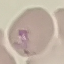

{
  "result": "no malaria parasites detected",
  "stain": "Giemsa",
  "image_type": "cell patch, automatically extracted from a larger field of view and resized to 64 × 64 pixels",
  "preparation": "thin blood film",
  "capture": "smartphone camera at the microscope eyepiece"
}